Describe the morphology of the erythrocytes.
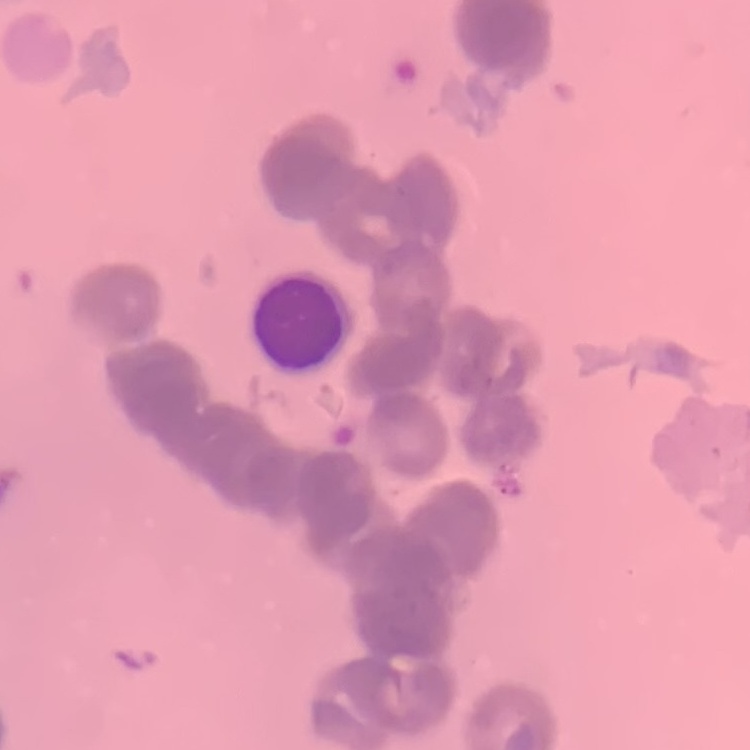
Rouleaux formation.

One tile cut from a larger photomicrograph. Thin peripheral smear. Field's or Giemsa stain.